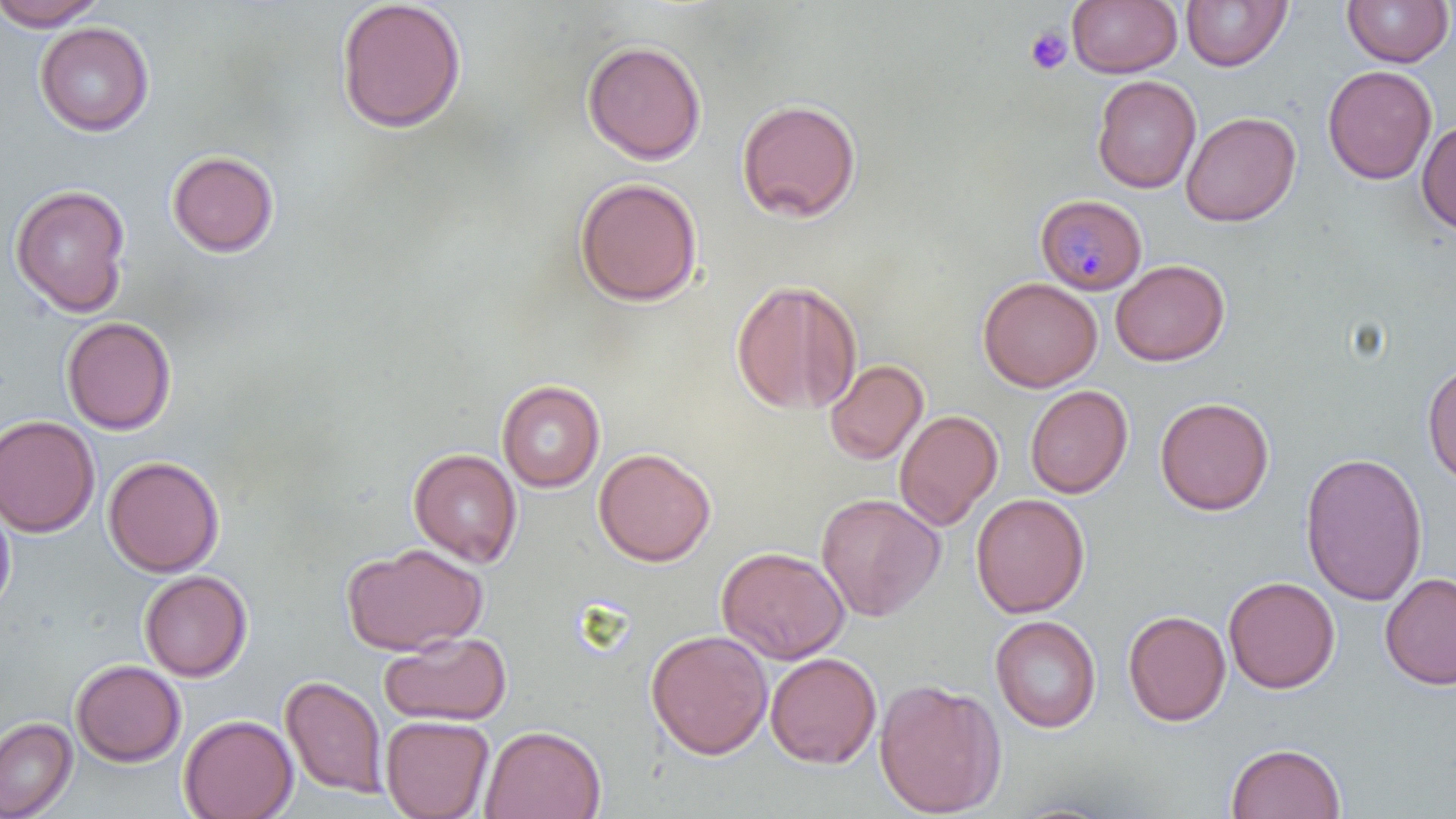
Summary:
  - Coordinate format: approximate bounding boxes as [x1, y1, x2, y2] in pixels
  - Uninfected red blood cell locations: [0, 0, 107, 30], [335, 0, 467, 134], [1181, 0, 1291, 71], [1342, 0, 1454, 67], [1067, 1, 1182, 78], [35, 21, 154, 136], [582, 40, 707, 164], [1322, 65, 1436, 184], [1091, 75, 1201, 193], [736, 98, 862, 223], [1180, 111, 1301, 227], [1417, 120, 1456, 235], [167, 149, 279, 257], [573, 176, 703, 307], [10, 184, 131, 317], [1110, 259, 1229, 366], [977, 277, 1102, 392], [730, 279, 862, 415], [61, 316, 177, 435], [825, 359, 928, 466], [1422, 359, 1455, 488], [497, 379, 605, 492], [1025, 385, 1133, 498], [1155, 396, 1274, 516], [894, 408, 1003, 530], [0, 415, 100, 537], [593, 447, 716, 567], [408, 448, 522, 566], [1299, 451, 1429, 606], [103, 455, 225, 577], [816, 493, 944, 621], [970, 493, 1089, 618], [0, 497, 16, 619], [342, 543, 488, 655], [716, 545, 849, 664], [139, 570, 252, 681], [1379, 572, 1456, 690], [1223, 576, 1339, 693], [1123, 610, 1231, 726], [989, 615, 1101, 733], [646, 629, 773, 760], [380, 632, 512, 726], [765, 652, 882, 768], [71, 659, 185, 766], [280, 674, 387, 798], [873, 678, 1007, 817], [179, 713, 298, 819], [381, 715, 494, 819], [0, 717, 77, 819], [479, 724, 606, 819], [1225, 742, 1346, 819]
  - Platelet locations: [1025, 26, 1073, 74]
  - Plasmodium malariae-infected red blood cell locations: [1035, 193, 1148, 294]
  - Slide-level diagnosis: Plasmodium malariae
  - Stain: May-Grünwald-Giemsa
  - Field of view: one of a larger specimen
  - Modality: light microscopy
  - Preparation: thin blood smear
  - Image size: 1456×819 pixels
  - Magnification: 1000x